Classify this cell by malaria status.
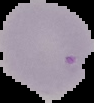

It is uninfected.

Image is 94×103 pixels. Cell region segmented out of the field of view; the surrounding area is masked to black. From a thin blood smear.